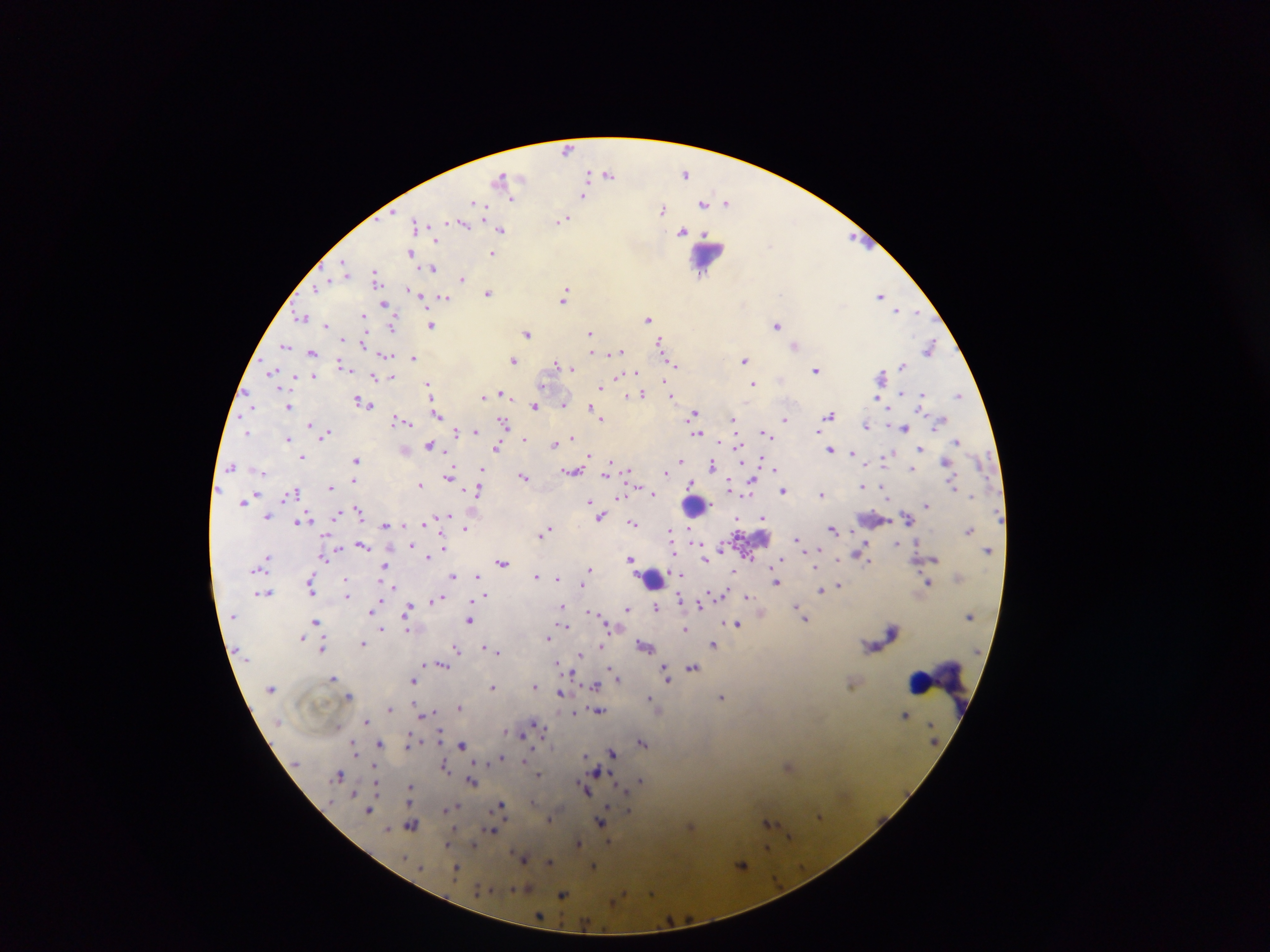
Approximate centers as x y in pixels. Leukocyte locations: 707 255; 695 505; 652 579; 937 680. Plasmodium parasite locations: 567 150; 686 173; 608 174; 504 178; 583 194; 511 197; 728 201; 704 203; 475 204; 662 209; 564 218; 463 223; 418 224; 502 230; 684 231; 686 232; 855 238; 411 253; 493 253; 344 268; 432 268; 377 277; 462 278; 317 286; 408 289; 415 292; 488 292; 566 294; 882 295; 423 297; 444 298; 384 303; 898 310; 909 311; 916 312; 364 314; 303 317; 648 318; 327 324; 431 324; 777 325; 394 326; 527 333; 590 333; 345 338; 660 343; 285 345; 363 345; 795 345; 930 347; 595 352; 618 352; 312 353; 385 354; 413 357; 514 359; 744 360; 343 364; 557 364; 676 364; 902 365; 572 368; 817 369; 272 371; 635 372; 882 375; 313 377; 392 377; 618 377; 377 378; 663 380; 544 382; 753 383; 429 384; 601 386; 903 391; 502 392; 923 393; 643 394; 483 396; 626 396; 672 396; 959 396; 878 397; 363 403; 564 403; 289 406; 535 407; 596 411; 438 413; 694 414; 830 414; 601 417; 785 418; 734 419; 398 420; 408 422; 503 423; 310 424; 866 426; 905 427; 474 431; 819 431; 248 432; 457 432; 697 433; 766 433; 328 434; 288 438; 573 438; 524 439; 958 441; 431 443; 555 443; 498 445; 920 447; 831 449; 853 453; 889 454; 590 455; 303 458; 759 458; 356 459; 743 460; 681 461; 946 463; 713 464; 867 464; 231 466; 912 468; 774 469; 482 470; 629 470; 572 471; 263 472; 607 473; 665 473; 523 475; 450 476; 354 480; 692 482; 729 484; 420 485; 863 486; 330 487; 639 487; 478 490; 783 490; 887 490; 296 492; 654 493; 748 493; 821 494; 255 495; 618 496; 243 502; 590 502; 926 504; 358 509; 337 514; 447 514; 602 516; 268 517; 765 517; 304 518; 736 519; 910 520; 299 521; 427 522; 633 522; 385 525; 405 526; 465 528; 833 529; 550 530; 969 530; 671 531; 544 532; 326 536; 798 538; 443 539; 897 543; 411 544; 362 545; 673 547; 339 548; 866 548; 444 549; 989 550; 817 551; 863 552; 673 553; 429 556; 324 558; 838 558; 932 558; 267 559; 630 559; 780 559; 705 560; 502 563; 385 566; 590 567; 735 570; 478 575; 537 576; 452 577; 347 578; 556 578; 383 582; 777 582; 928 582; 311 583; 583 583; 391 585; 838 585; 312 590; 820 591; 266 592; 486 595; 747 596; 347 598; 438 598; 681 598; 700 604; 562 606; 797 606; 656 607; 408 608; 627 608; 372 612; 591 612; 805 618; 469 620; 316 622; 736 624; 563 625; 608 627; 685 628; 382 629; 407 630; 894 630; 303 637; 548 637; 363 644; 713 644; 645 646; 323 647; 485 647; 601 647; 457 650; 492 650; 498 652; 581 654; 579 658; 557 662; 426 663; 441 664; 693 667; 665 668; 570 669; 612 672; 573 673; 667 674; 616 676; 334 677; 413 679; 535 686; 594 686; 493 687; 561 692; 348 696; 649 696; 721 696; 460 707; 390 708; 599 710; 431 712; 573 714; 906 714; 425 715; 367 719; 538 726; 505 732; 520 734; 441 738; 643 742; 380 743; 409 743; 354 745; 462 745; 612 753; 586 756; 502 758; 376 766; 444 766; 789 766; 598 772; 340 774; 538 774; 641 780; 472 782; 376 785; 621 786; 410 787; 585 790; 354 792; 456 806; 502 806; 370 809; 629 810; 820 816; 550 819; 768 821; 602 822; 411 824; 691 826; 492 827; 387 830; 789 837; 579 842; 609 843; 473 844; 448 845; 767 846; 523 857; 549 862; 742 865; 593 866; 457 867; 525 888; 516 891; 652 891; 563 894; 618 899; 540 917. Thick blood film. Photographed through a microscope with a mobile-phone camera. Image is 1270×952 pixels. Sample from Ghana. One field of view.